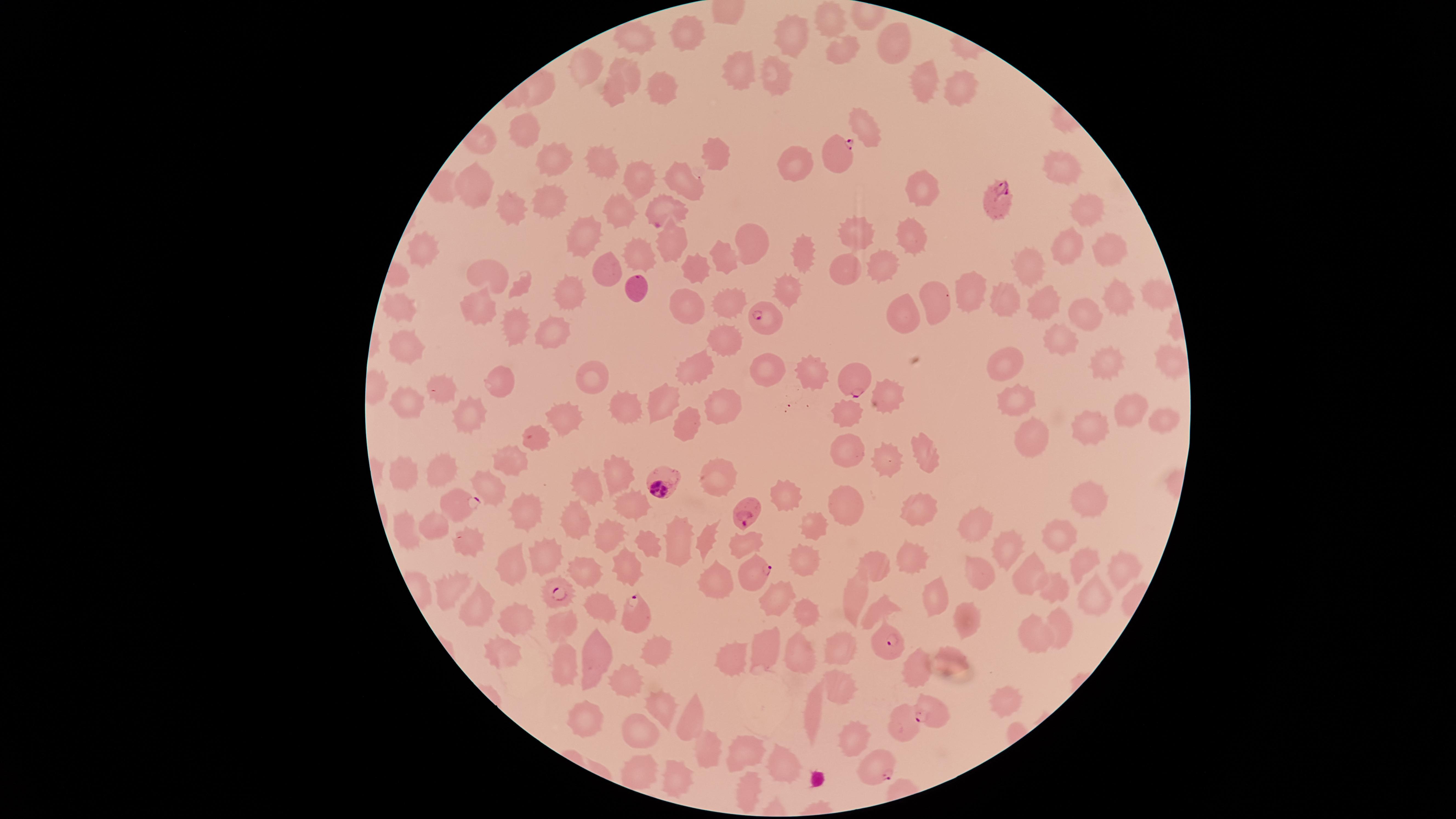
Approximate marker points as {x, y} in pixels. Parasitized red blood cells: {837, 157}, {997, 199}, {663, 213}, {638, 288}, {760, 316}, {849, 381}, {667, 481}, {460, 504}, {746, 516}, {753, 576}, {563, 592}, {631, 611}, {891, 645}, {929, 709}, {882, 769}. Uninfected red blood cells: {832, 22}, {686, 31}, {791, 35}, {635, 37}, {895, 43}, {844, 50}, {746, 64}, {779, 72}, {628, 74}, {924, 82}, {661, 86}, {964, 89}, {614, 95}, {864, 129}, {526, 130}, {714, 153}, {554, 157}, {601, 165}, {801, 166}, {1062, 171}, {686, 180}, {637, 182}, {475, 189}, {918, 189}, {546, 205}, {514, 210}, {622, 213}, {1082, 216}, {856, 234}, {911, 234}, {588, 235}, {1069, 238}, {750, 239}, {674, 243}, {420, 251}, {804, 251}, {1108, 253}, {634, 258}, {725, 259}, {885, 261}, {1029, 263}, {844, 264}, {697, 265}, {607, 273}, {484, 278}, {789, 287}, {966, 292}, {572, 293}, {1158, 294}, {936, 297}, {1006, 297}, {1115, 297}, {686, 302}, {398, 303}, {729, 303}, {1042, 304}, {478, 307}, {902, 307}, {1083, 315}, {515, 328}, {553, 332}, {1062, 338}, {403, 342}, {723, 342}, {1006, 358}, {1165, 363}, {1114, 364}, {769, 371}, {698, 372}, {498, 376}, {813, 376}, {588, 381}, {442, 391}, {1015, 394}, {407, 396}, {887, 400}, {617, 402}, {661, 402}, {720, 404}, {1134, 408}, {470, 412}, {563, 412}, {843, 414}, {1160, 418}, {686, 419}, {1094, 420}, {1037, 433}, {533, 436}, {848, 445}, {923, 449}, {886, 454}, {510, 459}, {617, 472}, {439, 474}, {406, 475}, {716, 478}, {491, 483}, {585, 488}, {787, 498}, {1089, 503}, {637, 506}, {524, 507}, {911, 508}, {843, 514}, {576, 516}, {438, 525}, {809, 528}, {978, 531}, {411, 534}, {1060, 534}, {608, 536}, {680, 538}, {705, 539}, {652, 543}, {473, 545}, {745, 545}, {1007, 548}, {542, 549}, {907, 556}, {878, 563}, {1081, 563}, {799, 564}, {512, 567}, {582, 569}, {625, 570}, {1119, 572}, {980, 573}, {1037, 576}, {716, 583}, {855, 590}, {1062, 590}, {450, 593}, {934, 593}, {777, 598}, {1088, 598}, {593, 610}, {877, 612}, {475, 613}, {969, 616}, {515, 617}, {805, 619}, {556, 622}, {1055, 629}, {1030, 634}, {845, 645}, {762, 647}, {795, 650}, {953, 655}, {503, 656}, {660, 657}, {555, 660}, {592, 663}, {734, 664}, {917, 666}, {838, 681}, {627, 683}, {1007, 699}, {816, 705}, {662, 713}, {692, 713}, {585, 720}, {900, 723}, {642, 731}, {846, 738}, {705, 745}, {744, 751}, {779, 760}, {679, 773}, {631, 774}, {744, 786}. One field of view of the specimen. Smartphone photograph through the microscope eyepiece. Species: Plasmodium falciparum. Giemsa stain. Image is 1456×819 pixels. Circular visible region. Presence: malaria parasites seen. Thin blood film.